Outline each Plasmodium falciparum-infected red blood cell.
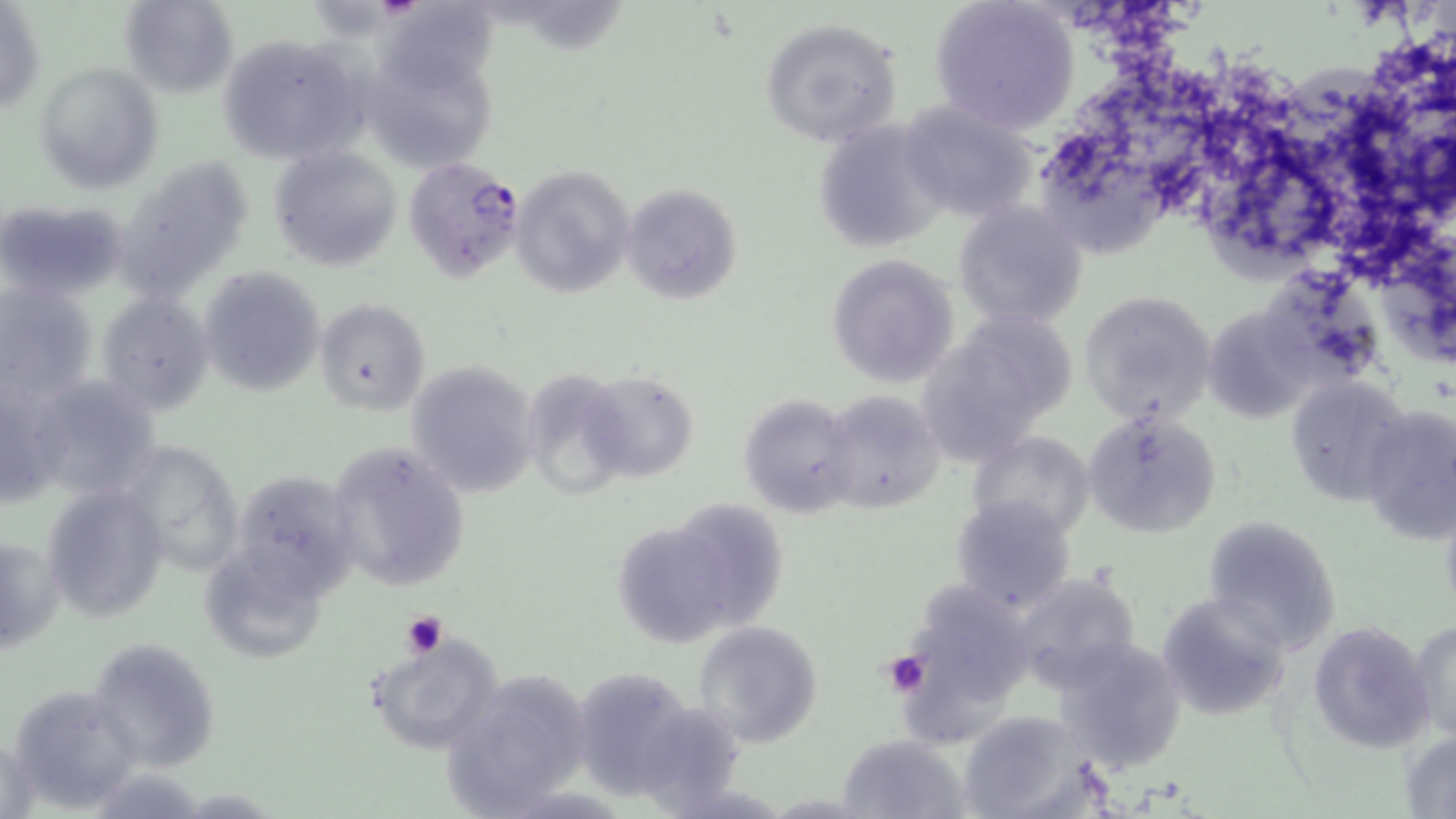
Approximate bounding boxes as (x1, y1, x2, y2) in pixels.
Plasmodium falciparum-infected red blood cells: (404, 155, 525, 283).

Summary:
  - Platelet locations: (402, 610, 448, 658), (881, 652, 931, 697)
  - Uninfected red blood cell locations: (119, 0, 239, 97), (928, 0, 1078, 132), (1, 3, 45, 121), (757, 16, 906, 150), (216, 33, 369, 164), (359, 33, 513, 172), (36, 62, 163, 194), (899, 99, 1040, 224), (812, 117, 953, 254), (270, 144, 403, 271), (126, 155, 256, 296), (508, 164, 632, 298), (619, 182, 741, 306), (0, 199, 123, 305), (955, 199, 1090, 331), (826, 253, 960, 388), (201, 268, 326, 397), (0, 282, 97, 402), (1078, 289, 1218, 428), (96, 290, 217, 415), (316, 297, 430, 415), (968, 303, 1083, 413), (1201, 304, 1321, 424), (912, 345, 1034, 468), (406, 360, 540, 499), (581, 370, 700, 482), (1286, 374, 1411, 507), (24, 375, 166, 505), (0, 379, 62, 509), (819, 391, 946, 515), (737, 392, 860, 517), (1357, 404, 1456, 543), (1084, 410, 1221, 538), (968, 430, 1097, 541), (119, 439, 246, 574), (324, 439, 471, 592), (39, 480, 168, 623), (263, 485, 367, 591), (949, 495, 1077, 617), (684, 503, 796, 625), (1201, 514, 1344, 654), (618, 528, 735, 649), (1, 529, 60, 657), (205, 548, 324, 666), (1010, 572, 1144, 695), (1155, 590, 1291, 720), (906, 602, 1020, 737), (1409, 616, 1456, 740), (1307, 619, 1435, 754), (690, 622, 824, 748), (367, 633, 505, 756), (86, 636, 221, 774), (1053, 637, 1189, 777), (439, 671, 594, 819), (593, 681, 701, 800), (7, 684, 145, 811), (958, 709, 1098, 817), (1399, 730, 1456, 816), (838, 734, 966, 819)
  - Slide-level diagnosis: Plasmodium falciparum
  - Image size: 1456×819 pixels
  - Stain: May-Grünwald-Giemsa
  - Preparation: thin blood smear
  - Modality: optical microscopy
  - Field of view: one of a larger specimen
  - Magnification: 1000x